Assess this cell for malaria.
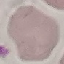

Uninfected.

Giemsa-stained preparation. Photographed with a smartphone camera at the microscope eyepiece. Thin blood smear. Automatically extracted cell patch, resized to 64 × 64 pixels.